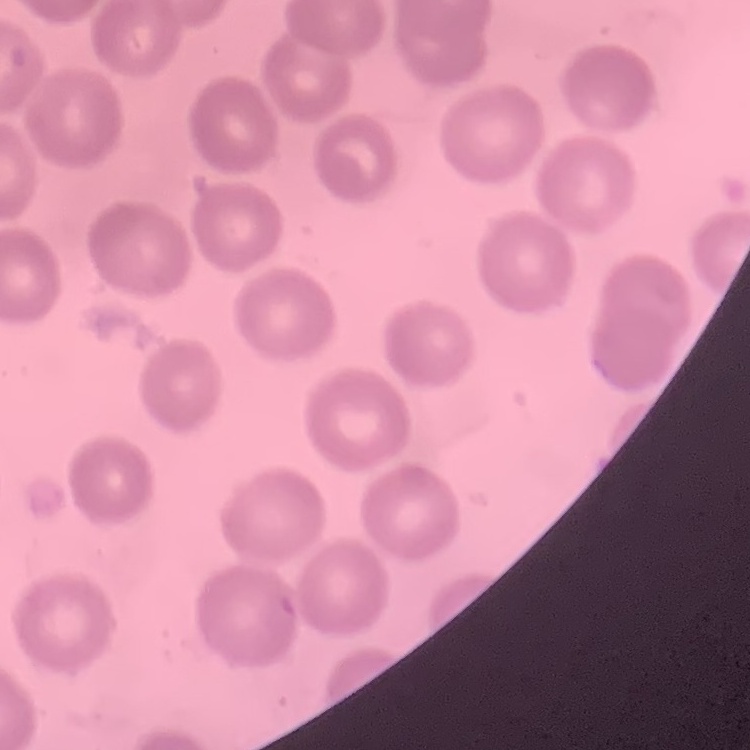

Summary:
  - Erythrocyte morphology: no rouleaux formation
  - Image type: one tile cut from a larger photomicrograph
  - Stain: Field's or Giemsa
  - Preparation: thin blood film